Locate every blood parasite and identify its species.
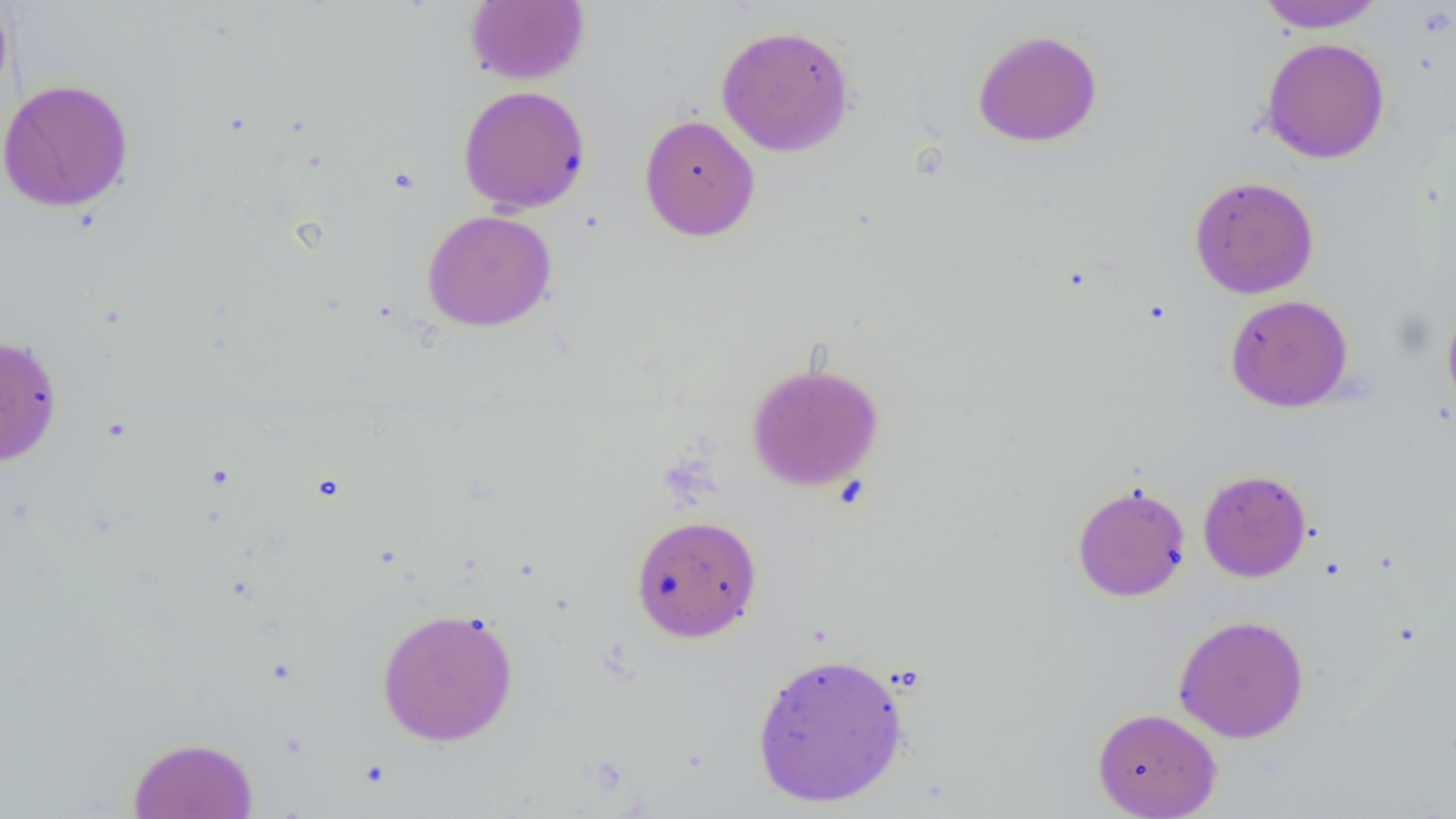

No blood parasites seen.

Summary:
  - Coordinate format: approximate bounding boxes as named x1/y1/x2/y2 corners in pixels
  - Uninfected red blood cell locations: (x1=1254, y1=0, x2=1388, y2=33), (x1=0, y1=1, x2=14, y2=108), (x1=465, y1=1, x2=589, y2=85), (x1=715, y1=24, x2=855, y2=157), (x1=971, y1=29, x2=1103, y2=148), (x1=1260, y1=37, x2=1390, y2=164), (x1=0, y1=78, x2=134, y2=213), (x1=458, y1=85, x2=592, y2=214), (x1=639, y1=114, x2=760, y2=241), (x1=1188, y1=176, x2=1319, y2=299), (x1=422, y1=209, x2=557, y2=332), (x1=1225, y1=294, x2=1353, y2=412), (x1=1441, y1=302, x2=1456, y2=419), (x1=0, y1=334, x2=63, y2=467), (x1=745, y1=361, x2=884, y2=491), (x1=1197, y1=469, x2=1312, y2=582), (x1=1071, y1=481, x2=1191, y2=602), (x1=630, y1=514, x2=763, y2=642), (x1=375, y1=607, x2=520, y2=747), (x1=1173, y1=614, x2=1310, y2=743), (x1=750, y1=651, x2=910, y2=809), (x1=1092, y1=707, x2=1222, y2=819), (x1=127, y1=736, x2=259, y2=819)
  - Slide-level diagnosis: no evidence of blood parasites
  - Image size: 1456×819 pixels
  - Field of view: one of a larger specimen
  - Magnification: 1000x
  - Modality: optical microscopy
  - Preparation: thin blood film